Point out each Plasmodium parasite.
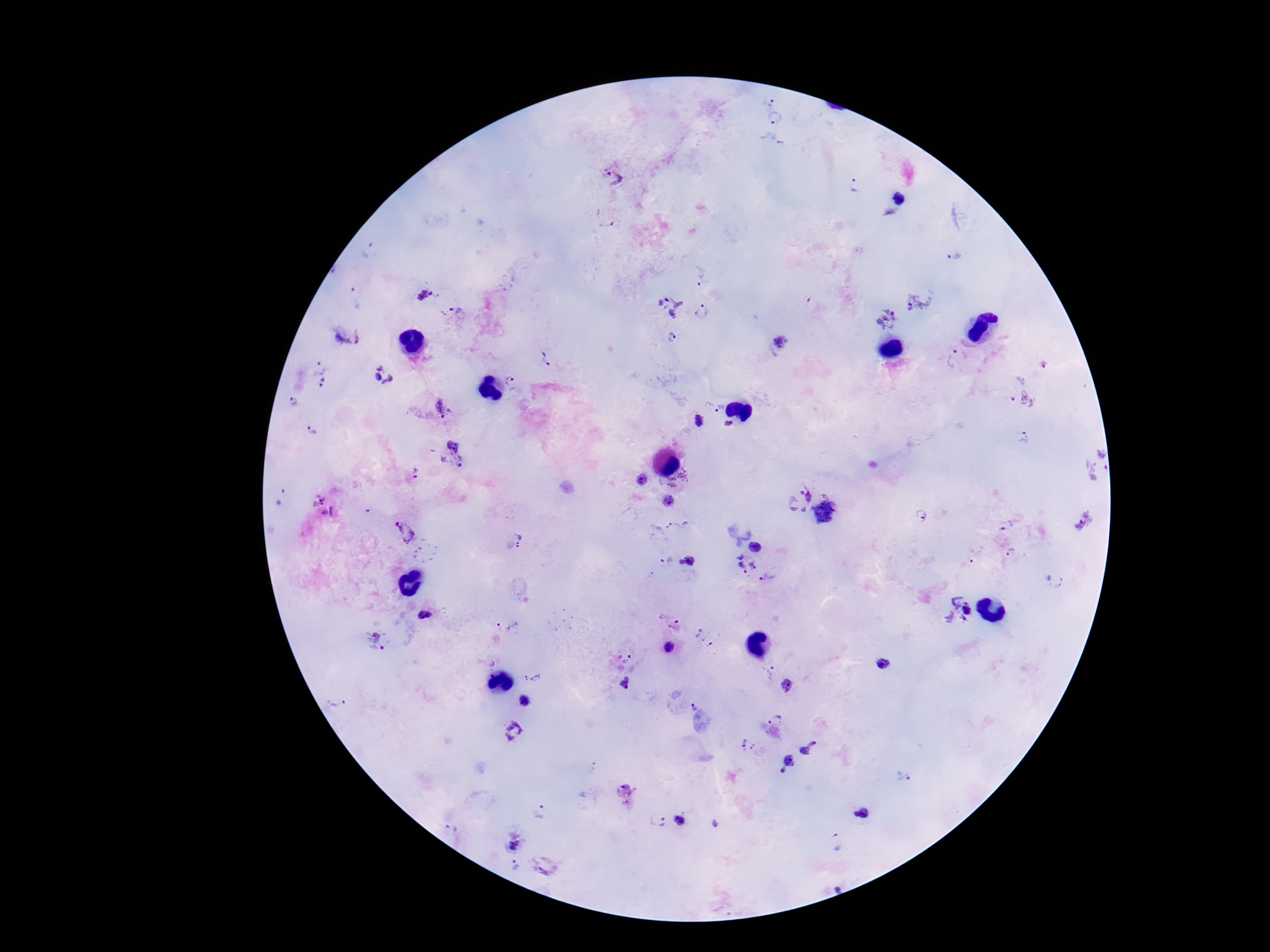

Approximate centers as [x, y] in pixels.
Plasmodium parasites: [769, 100], [775, 120], [771, 144], [614, 178], [855, 187], [900, 200], [606, 223], [369, 251], [952, 255], [703, 275], [424, 294], [355, 299], [918, 301], [670, 306], [458, 310], [702, 312], [886, 320], [349, 338], [672, 339], [781, 342], [546, 358], [956, 359], [1045, 365], [319, 366], [386, 376], [510, 382], [323, 385], [1020, 399], [295, 402], [443, 409], [719, 409], [700, 422], [729, 423], [312, 431], [1024, 437], [454, 453], [1093, 465], [415, 473], [644, 480], [682, 483], [282, 496], [798, 499], [669, 500], [323, 507], [824, 512], [921, 516], [1080, 520], [1007, 525], [676, 526], [406, 531], [520, 541], [757, 547], [1010, 551], [975, 555], [741, 556], [688, 560], [666, 561], [754, 565], [741, 569], [769, 578], [958, 609], [425, 615], [509, 625], [674, 626], [705, 637], [377, 640], [670, 647], [624, 658], [492, 663], [882, 664], [767, 672], [532, 677], [626, 683], [785, 686], [339, 701], [524, 701], [694, 706], [776, 720], [513, 731], [742, 744], [809, 748], [756, 749], [786, 766], [902, 775], [626, 793], [539, 811], [861, 814], [658, 820], [680, 821], [716, 824], [450, 830], [835, 842], [514, 845], [545, 864], [515, 865].

Summary:
  - Stain: Giemsa
  - Preparation: thick blood smear
  - Field of view: single
  - Patient malaria status: infected
  - Image size: 1270×952 pixels
  - Capture: smartphone camera through the microscope eyepiece
  - Magnification: 100x